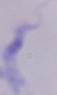 Captured at 1000x magnification. Micrograph. A trypanosome is seen.